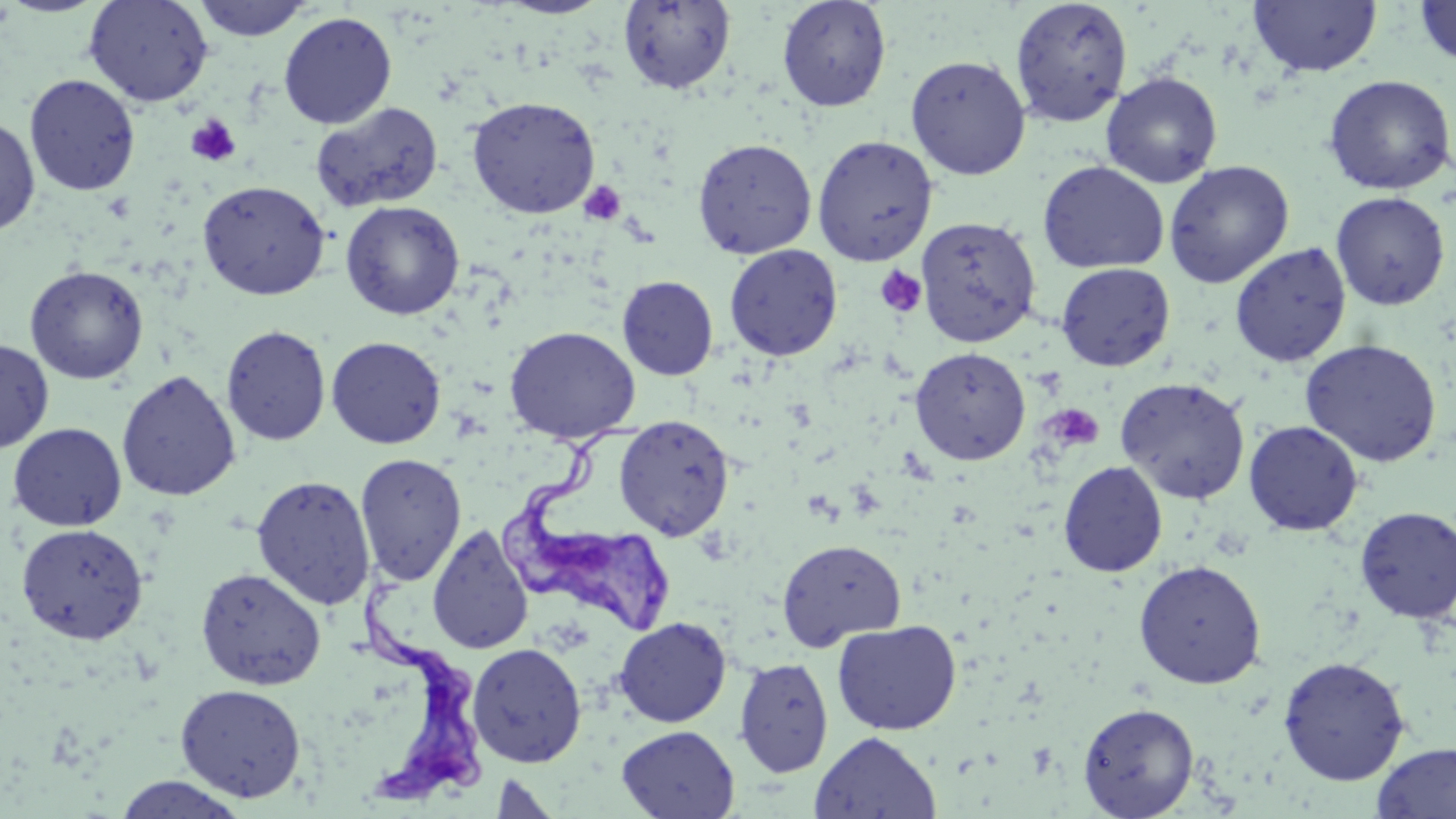

slide-level diagnosis = Trypanosoma brucei
magnification = 1000x
field of view = single
platelet locations = approximate bounding boxes as (x1, y1, x2, y2) in pixels: (186, 114, 241, 167), (580, 180, 626, 226), (874, 265, 926, 318), (1046, 404, 1103, 450)
preparation = thin blood smear
image size = 1456×819 pixels
modality = light microscopy
stain = May-Grünwald-Giemsa
Trypanosoma brucei locations = approximate bounding boxes as (x1, y1, x2, y2) in pixels: (498, 417, 681, 640), (357, 570, 490, 806)
uninfected red blood cell locations = approximate bounding boxes as (x1, y1, x2, y2) in pixels: (83, 0, 214, 107), (193, 0, 314, 42), (776, 0, 892, 112), (1009, 0, 1133, 126), (1247, 0, 1383, 77), (1413, 0, 1456, 68), (618, 1, 737, 95), (278, 11, 397, 128), (905, 54, 1031, 180), (1101, 71, 1223, 188), (24, 73, 141, 196), (1323, 75, 1455, 195), (466, 96, 601, 218), (310, 101, 444, 213), (0, 114, 40, 236), (812, 134, 938, 265), (692, 138, 817, 258), (1037, 160, 1170, 274), (1164, 160, 1295, 288), (197, 179, 330, 300), (1330, 191, 1451, 311), (340, 200, 465, 320), (916, 216, 1041, 348), (1230, 242, 1351, 366), (724, 244, 843, 361), (1056, 262, 1175, 371), (24, 265, 149, 384), (617, 276, 719, 381), (221, 325, 332, 446), (504, 325, 641, 443), (326, 336, 446, 449), (0, 337, 54, 454), (1300, 338, 1442, 467), (909, 346, 1031, 465), (116, 369, 241, 502), (1115, 376, 1250, 504), (613, 414, 735, 540), (1243, 420, 1364, 536), (7, 422, 127, 531), (355, 453, 467, 585), (1058, 460, 1168, 577), (251, 475, 376, 610), (1355, 506, 1456, 625), (15, 522, 149, 645), (427, 523, 534, 655), (776, 539, 907, 650), (1133, 559, 1267, 689), (195, 567, 327, 690), (613, 616, 732, 727), (832, 619, 962, 735), (467, 643, 586, 767), (1277, 656, 1410, 785), (733, 657, 834, 778), (175, 683, 306, 801), (1078, 702, 1200, 818), (617, 725, 739, 818), (810, 731, 941, 819), (1372, 742, 1456, 818), (489, 772, 561, 819), (111, 775, 251, 818)